Outline each Plasmodium vivax-infected red blood cell.
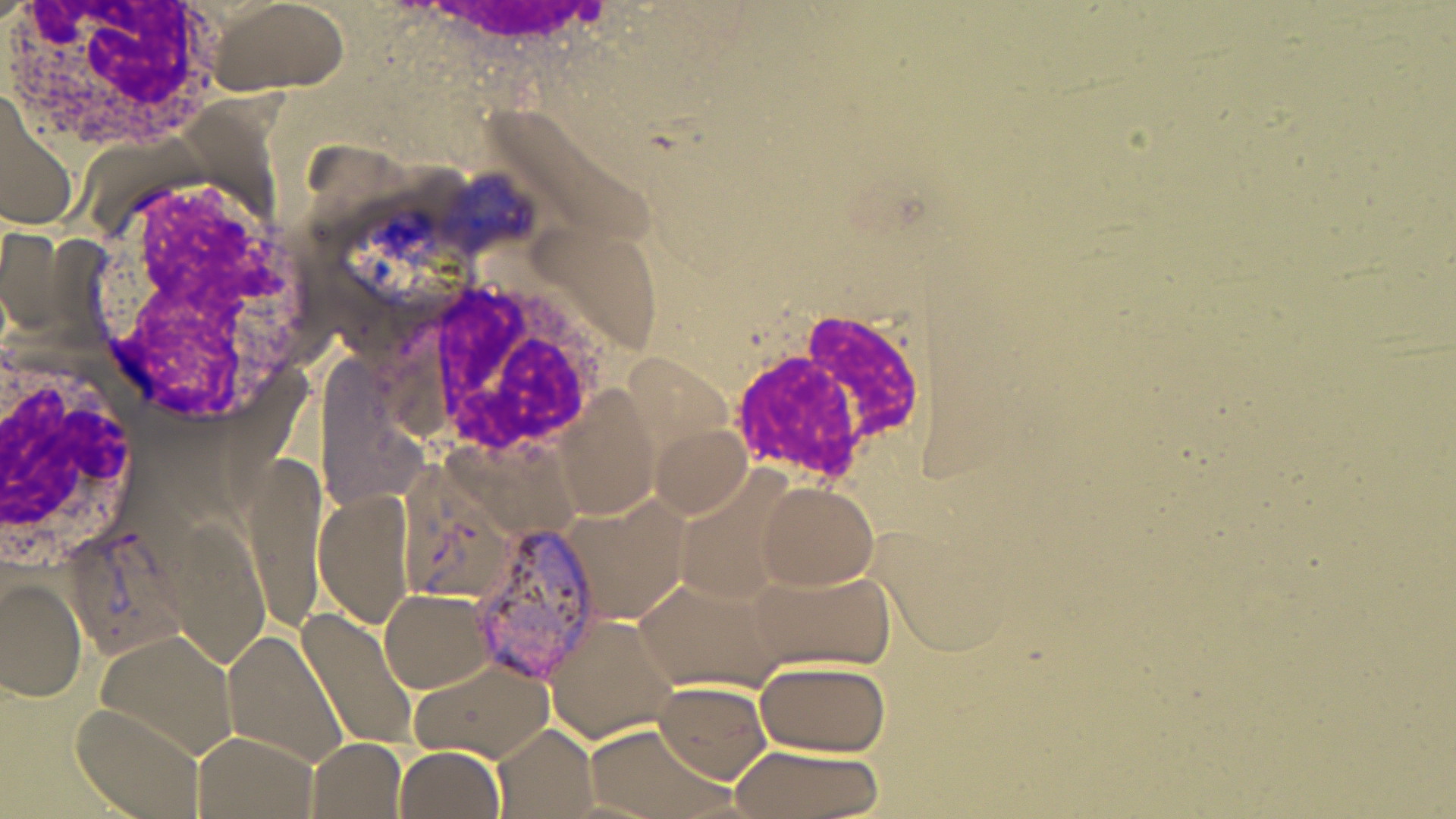

Approximate bounding boxes as named x1/y1/x2/y2 corners in pixels.
Plasmodium vivax-infected red blood cells: (x1=467, y1=520, x2=610, y2=685), (x1=60, y1=524, x2=186, y2=662).

Summary:
  - Uninfected red blood cell locations: (x1=200, y1=0, x2=349, y2=100), (x1=0, y1=89, x2=78, y2=231), (x1=556, y1=387, x2=663, y2=518), (x1=650, y1=422, x2=752, y2=520), (x1=244, y1=455, x2=328, y2=629), (x1=754, y1=481, x2=880, y2=590), (x1=314, y1=486, x2=419, y2=630), (x1=562, y1=495, x2=694, y2=625), (x1=162, y1=517, x2=270, y2=670), (x1=873, y1=521, x2=1021, y2=655), (x1=746, y1=567, x2=893, y2=668), (x1=1, y1=574, x2=87, y2=703), (x1=632, y1=576, x2=781, y2=696), (x1=378, y1=588, x2=498, y2=693), (x1=295, y1=606, x2=422, y2=753), (x1=541, y1=614, x2=681, y2=745), (x1=96, y1=628, x2=241, y2=762), (x1=224, y1=628, x2=347, y2=768), (x1=753, y1=656, x2=891, y2=756), (x1=410, y1=660, x2=554, y2=762), (x1=650, y1=679, x2=773, y2=782), (x1=70, y1=706, x2=206, y2=819), (x1=579, y1=722, x2=735, y2=819), (x1=494, y1=726, x2=596, y2=816), (x1=190, y1=730, x2=319, y2=819), (x1=308, y1=736, x2=406, y2=818), (x1=727, y1=745, x2=882, y2=819), (x1=393, y1=746, x2=504, y2=819)
  - White blood cell locations: (x1=2, y1=0, x2=231, y2=156), (x1=81, y1=174, x2=326, y2=429), (x1=379, y1=278, x2=613, y2=462), (x1=722, y1=308, x2=936, y2=494), (x1=0, y1=348, x2=147, y2=564)
  - Slide-level diagnosis: Plasmodium vivax
  - Field of view: one of a larger specimen
  - Image size: 1456×819 pixels
  - Preparation: thin blood film
  - Stain: May-Grünwald-Giemsa
  - Magnification: 1000x
  - Modality: light microscopy